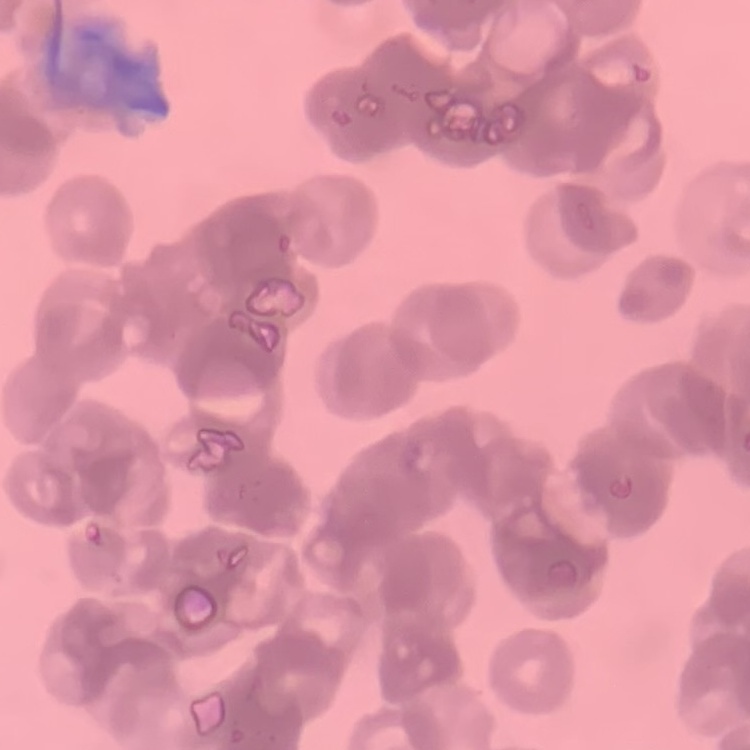
red blood cell morphology = rouleaux formation
stain = Field's or Giemsa
image type = one tile cut from a larger photomicrograph
preparation = thin peripheral smear